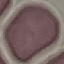
Summary:
  - Result: no malaria parasites detected
  - Preparation: thin smear
  - Capture: smartphone camera at the microscope eyepiece
  - Image type: cell patch, automatically extracted from a larger field of view and resized to 64 × 64 pixels
  - Stain: Giemsa